Name the blood parasite species.
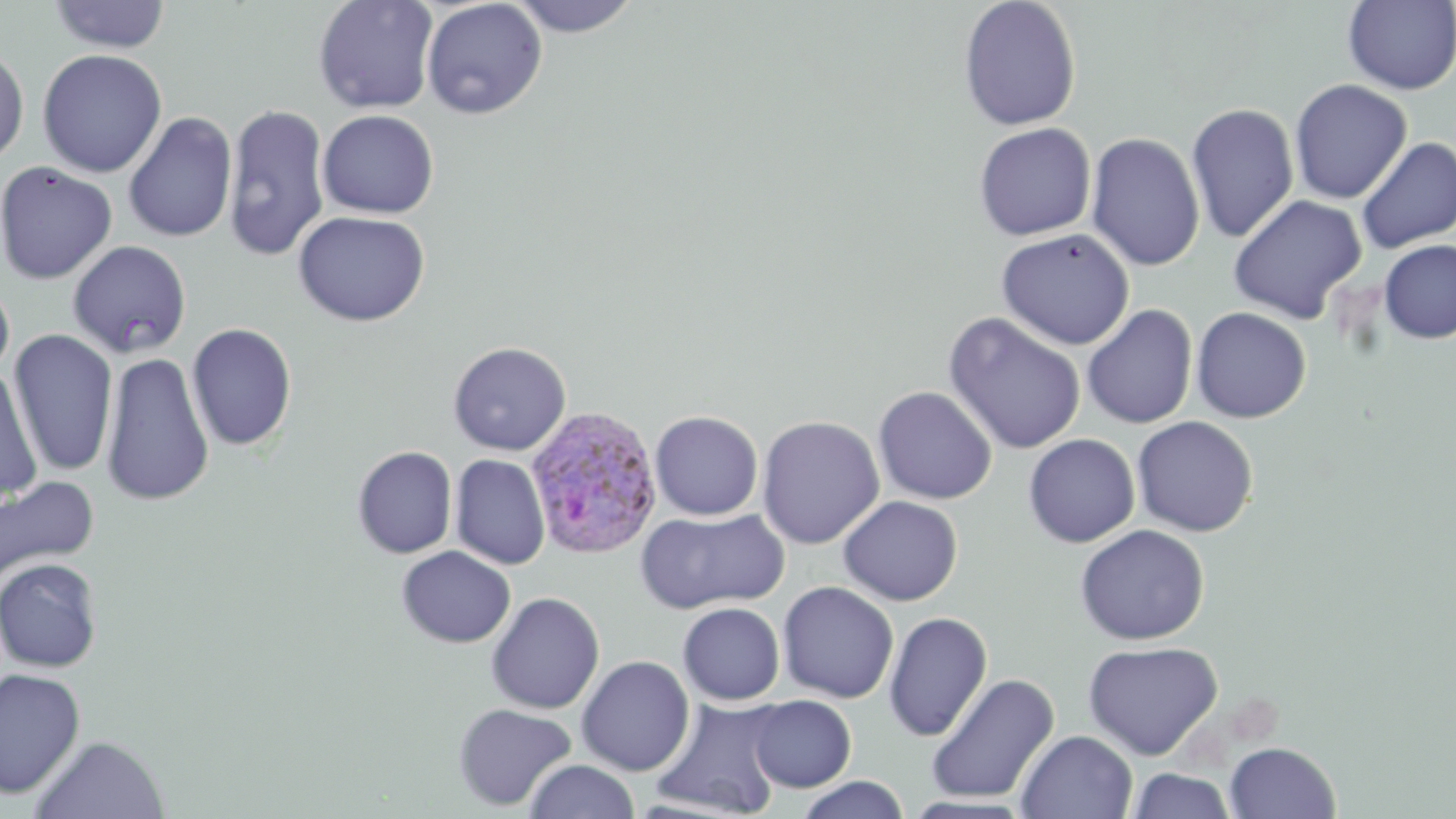

Plasmodium ovale.

Approximate bounding boxes as [x1, y1, x2, y2] in pixels. Plasmodium ovale-infected red blood cell locations: [525, 405, 663, 558]. Uninfected red blood cell locations: [313, 0, 440, 114], [506, 0, 644, 37], [957, 0, 1082, 131], [46, 1, 173, 54], [421, 1, 548, 119], [1343, 1, 1455, 95], [0, 43, 29, 166], [37, 48, 167, 178], [1289, 79, 1412, 204], [1186, 102, 1300, 244], [222, 103, 331, 261], [317, 109, 440, 218], [122, 111, 237, 243], [973, 122, 1096, 241], [1086, 132, 1205, 271], [1356, 137, 1456, 254], [0, 161, 118, 284], [1228, 194, 1367, 324], [293, 210, 430, 327], [995, 228, 1136, 349], [1377, 239, 1456, 344], [68, 240, 191, 358], [0, 276, 15, 384], [1082, 304, 1198, 429], [1191, 306, 1312, 423], [943, 312, 1087, 455], [186, 322, 298, 452], [7, 329, 118, 475], [447, 341, 572, 456], [100, 351, 214, 508], [0, 368, 42, 507], [873, 386, 997, 505], [650, 410, 763, 521], [756, 414, 885, 549], [1132, 416, 1259, 536], [1023, 433, 1140, 548], [352, 446, 457, 559], [450, 454, 550, 570], [0, 475, 99, 586], [838, 495, 963, 605], [636, 507, 788, 615], [1074, 524, 1211, 645], [396, 545, 516, 648], [0, 557, 104, 672], [777, 581, 899, 704], [485, 592, 604, 714], [677, 602, 785, 705], [883, 612, 992, 742], [1082, 639, 1223, 760], [576, 655, 695, 776], [0, 667, 85, 799], [925, 672, 1060, 804], [746, 695, 856, 792], [650, 696, 788, 818], [452, 703, 577, 811], [1016, 730, 1138, 819], [30, 734, 170, 819], [1224, 742, 1341, 819], [523, 759, 641, 819], [1126, 768, 1238, 819], [794, 776, 911, 819]. May-Grünwald-Giemsa-stained preparation. Optical microscopy. Image is 1456×819 pixels. Thin blood smear. 1000x magnification. One field of a larger specimen.